Outline each Trypanosoma brucei.
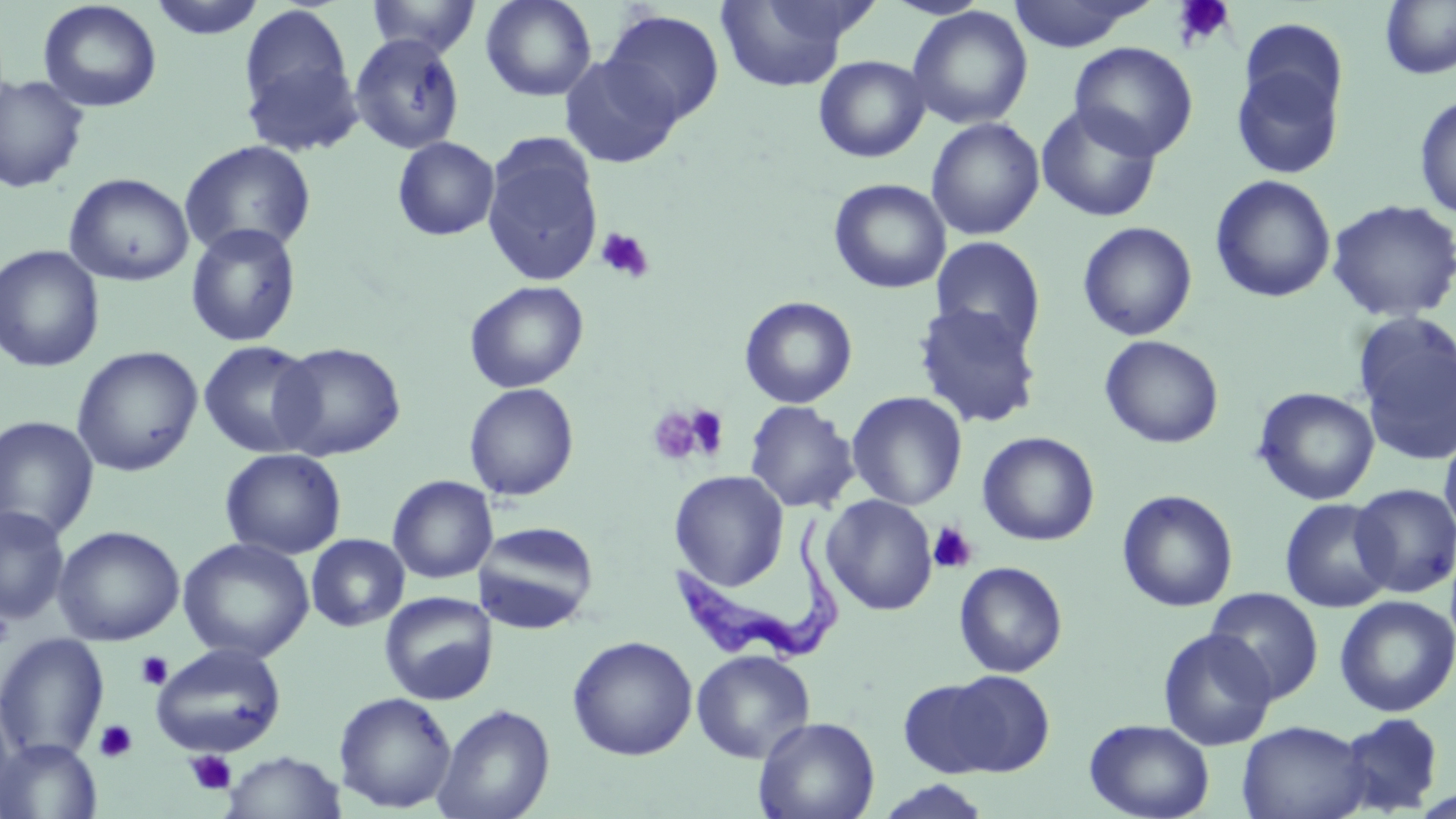
Approximate bounding boxes as [x1, y1, x2, y2] in pixels.
Trypanosoma brucei: [669, 517, 851, 669].

slide_level_diagnosis: Trypanosoma brucei
preparation: thin blood smear
uninfected_red_blood_cell_locations: 'approximate bounding boxes as [x1, y1, x2, y2] in pixels: [147, 0, 268, 41], [366, 0, 482, 58], [480, 0, 597, 102], [882, 0, 992, 19], [1006, 0, 1152, 51], [37, 1, 162, 113], [713, 1, 868, 92], [1380, 1, 1456, 79], [237, 3, 358, 141], [906, 6, 1033, 130], [601, 9, 725, 128], [348, 34, 466, 155], [1069, 42, 1198, 161], [1230, 50, 1346, 181], [558, 54, 684, 168], [813, 55, 930, 163], [0, 74, 91, 194], [1414, 94, 1456, 220], [1035, 103, 1163, 223], [926, 118, 1045, 240], [480, 134, 604, 287], [392, 136, 500, 241], [179, 140, 318, 259], [64, 172, 194, 287], [1211, 175, 1336, 304], [828, 178, 951, 294], [1326, 198, 1456, 323], [1077, 221, 1198, 341], [185, 223, 302, 347], [930, 236, 1046, 352], [0, 245, 105, 373], [464, 280, 589, 394], [739, 296, 858, 408], [912, 302, 1042, 429], [1352, 313, 1456, 466], [1099, 335, 1224, 449], [198, 340, 321, 458], [271, 342, 407, 461], [71, 345, 203, 477], [463, 383, 579, 501], [1253, 387, 1380, 505], [846, 391, 968, 510], [743, 400, 859, 513], [0, 415, 100, 541], [977, 431, 1100, 546], [1440, 431, 1456, 540], [220, 448, 347, 560], [669, 470, 789, 590], [387, 475, 498, 584], [1350, 483, 1456, 598], [1117, 489, 1239, 612], [821, 494, 938, 616], [1279, 497, 1396, 613], [0, 504, 70, 625], [473, 520, 600, 634], [53, 525, 185, 646], [306, 534, 410, 632], [178, 537, 314, 663], [954, 561, 1068, 678], [1205, 587, 1324, 703], [379, 591, 498, 705], [1334, 595, 1456, 718], [1157, 627, 1277, 750], [0, 633, 110, 761], [566, 635, 698, 761], [151, 642, 286, 757], [691, 649, 816, 764], [924, 670, 1056, 777], [0, 687, 20, 807], [334, 691, 457, 813], [432, 703, 556, 819], [1334, 713, 1443, 814], [753, 715, 880, 819], [1083, 718, 1215, 819], [1236, 720, 1371, 819], [0, 738, 102, 818], [221, 751, 347, 818], [873, 780, 994, 819]'
image_size: 1456×819 pixels
stain: May-Grünwald-Giemsa
field_of_view: one of a larger specimen
modality: light microscopy
magnification: 1000x
platelet_locations: 'approximate bounding boxes as [x1, y1, x2, y2] in pixels: [1172, 0, 1235, 49], [595, 227, 655, 283], [681, 403, 731, 460], [646, 406, 711, 466], [928, 522, 978, 574], [0, 608, 14, 650], [135, 651, 173, 690], [93, 719, 138, 763], [186, 750, 236, 795]'